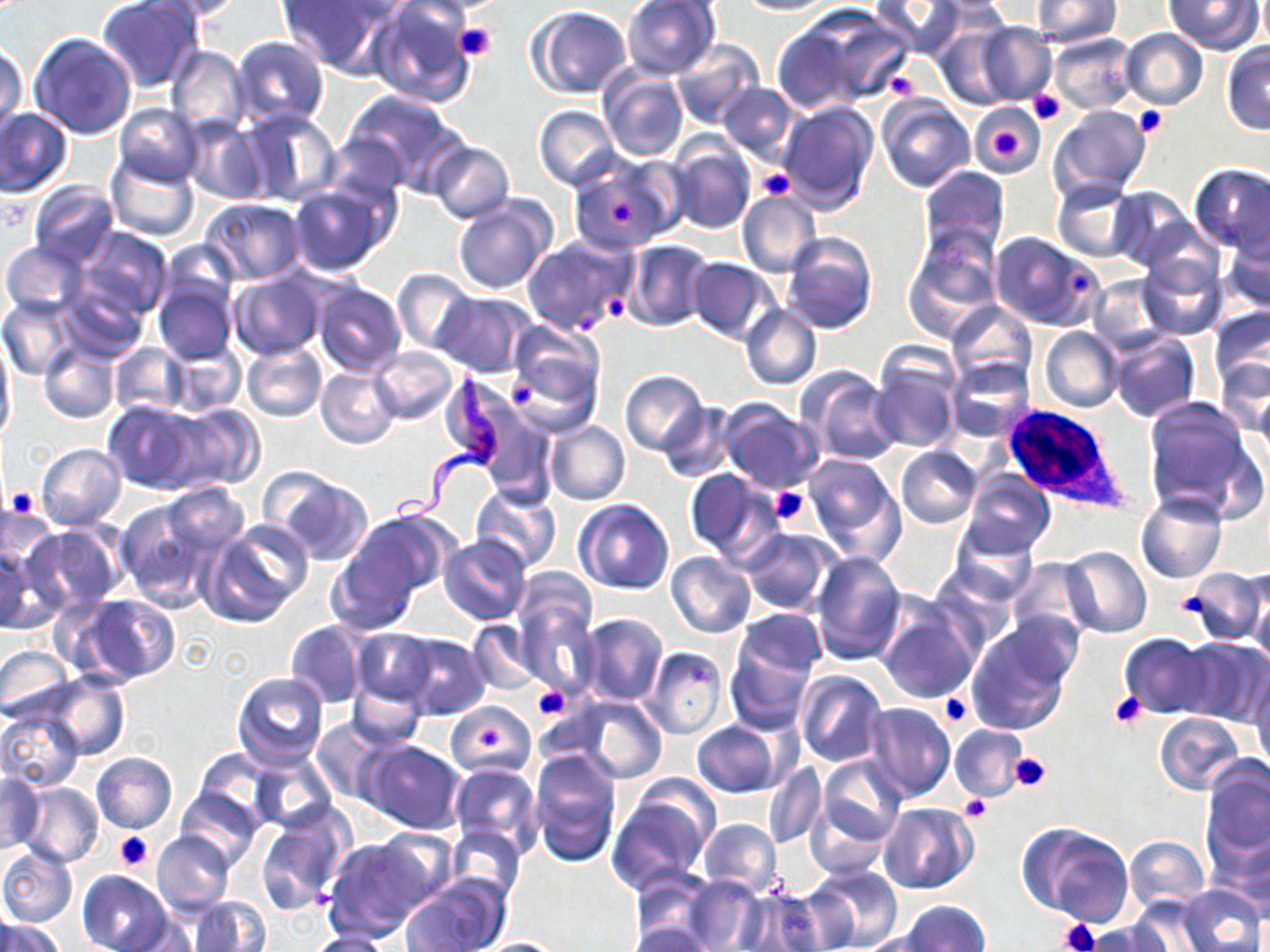
slide-level diagnosis = Trypanosoma brucei
stain = May-Grünwald-Giemsa
field of view = single
Trypanosoma brucei locations = approximate bounding boxes as named x1/y1/x2/y2 corners in pixels: (x1=388, y1=366, x2=505, y2=527)
platelet locations = approximate bounding boxes as named x1/y1/x2/y2 corners in pixels: (x1=452, y1=23, x2=497, y2=62), (x1=883, y1=67, x2=921, y2=100), (x1=1027, y1=90, x2=1064, y2=124), (x1=1133, y1=106, x2=1168, y2=139), (x1=991, y1=128, x2=1022, y2=160), (x1=755, y1=168, x2=793, y2=200), (x1=606, y1=201, x2=636, y2=225), (x1=1067, y1=269, x2=1093, y2=297), (x1=600, y1=291, x2=628, y2=323), (x1=504, y1=379, x2=541, y2=410), (x1=769, y1=486, x2=810, y2=526), (x1=6, y1=487, x2=39, y2=518), (x1=1177, y1=590, x2=1212, y2=622), (x1=531, y1=685, x2=572, y2=721), (x1=1109, y1=693, x2=1148, y2=729), (x1=939, y1=694, x2=974, y2=728), (x1=481, y1=725, x2=506, y2=749), (x1=1007, y1=752, x2=1050, y2=792), (x1=958, y1=794, x2=989, y2=823), (x1=115, y1=833, x2=152, y2=870), (x1=1058, y1=919, x2=1100, y2=952)
modality = optical microscopy
image size = 1270×952 pixels
uninfected red blood cell locations = approximate bounding boxes as named x1/y1/x2/y2 corners in pixels: (x1=96, y1=0, x2=206, y2=93), (x1=149, y1=0, x2=252, y2=20), (x1=277, y1=0, x2=394, y2=75), (x1=366, y1=0, x2=478, y2=107), (x1=621, y1=0, x2=721, y2=79), (x1=735, y1=0, x2=838, y2=16), (x1=870, y1=0, x2=964, y2=57), (x1=1030, y1=0, x2=1122, y2=46), (x1=1166, y1=0, x2=1262, y2=54), (x1=529, y1=7, x2=632, y2=99), (x1=808, y1=12, x2=913, y2=106), (x1=438, y1=19, x2=501, y2=63), (x1=967, y1=20, x2=1055, y2=105), (x1=771, y1=24, x2=866, y2=115), (x1=934, y1=24, x2=1018, y2=110), (x1=1120, y1=29, x2=1208, y2=109), (x1=28, y1=31, x2=139, y2=140), (x1=1048, y1=33, x2=1137, y2=114), (x1=231, y1=37, x2=329, y2=128), (x1=1, y1=40, x2=28, y2=139), (x1=671, y1=40, x2=764, y2=131), (x1=1220, y1=44, x2=1270, y2=135), (x1=167, y1=46, x2=249, y2=136), (x1=598, y1=70, x2=689, y2=163), (x1=717, y1=84, x2=799, y2=166), (x1=343, y1=88, x2=463, y2=188), (x1=877, y1=98, x2=974, y2=193), (x1=781, y1=101, x2=880, y2=213), (x1=114, y1=103, x2=202, y2=187), (x1=971, y1=104, x2=1045, y2=176), (x1=1046, y1=104, x2=1152, y2=202), (x1=533, y1=105, x2=620, y2=190), (x1=237, y1=107, x2=340, y2=206), (x1=0, y1=108, x2=73, y2=198), (x1=183, y1=119, x2=268, y2=205), (x1=325, y1=132, x2=408, y2=209), (x1=668, y1=140, x2=756, y2=235), (x1=427, y1=141, x2=514, y2=224), (x1=106, y1=155, x2=200, y2=243), (x1=570, y1=159, x2=681, y2=252), (x1=1187, y1=164, x2=1270, y2=252), (x1=917, y1=165, x2=1009, y2=259), (x1=1051, y1=179, x2=1138, y2=262), (x1=27, y1=182, x2=119, y2=270), (x1=287, y1=185, x2=391, y2=275), (x1=1107, y1=186, x2=1194, y2=270), (x1=738, y1=190, x2=822, y2=279), (x1=451, y1=196, x2=555, y2=295), (x1=201, y1=198, x2=306, y2=285), (x1=1143, y1=216, x2=1224, y2=297), (x1=1221, y1=219, x2=1270, y2=314), (x1=77, y1=227, x2=174, y2=318), (x1=781, y1=231, x2=879, y2=334), (x1=901, y1=231, x2=1000, y2=341), (x1=990, y1=231, x2=1101, y2=331), (x1=521, y1=235, x2=637, y2=337), (x1=161, y1=240, x2=241, y2=312), (x1=624, y1=241, x2=712, y2=331), (x1=2, y1=242, x2=88, y2=320), (x1=1138, y1=253, x2=1228, y2=340), (x1=686, y1=259, x2=778, y2=344), (x1=391, y1=269, x2=477, y2=355), (x1=227, y1=272, x2=326, y2=360), (x1=1085, y1=274, x2=1170, y2=356), (x1=57, y1=276, x2=148, y2=360), (x1=154, y1=280, x2=239, y2=365), (x1=313, y1=282, x2=405, y2=376), (x1=434, y1=292, x2=538, y2=377), (x1=0, y1=295, x2=79, y2=380), (x1=946, y1=301, x2=1037, y2=389), (x1=741, y1=303, x2=821, y2=391), (x1=1208, y1=306, x2=1270, y2=400), (x1=504, y1=319, x2=607, y2=426), (x1=1039, y1=327, x2=1124, y2=413), (x1=1107, y1=332, x2=1200, y2=424), (x1=0, y1=333, x2=15, y2=448), (x1=1122, y1=333, x2=1227, y2=474), (x1=39, y1=339, x2=119, y2=423), (x1=108, y1=342, x2=189, y2=418), (x1=242, y1=342, x2=327, y2=422), (x1=167, y1=344, x2=244, y2=415), (x1=371, y1=347, x2=458, y2=425), (x1=1214, y1=356, x2=1269, y2=437), (x1=871, y1=357, x2=960, y2=454), (x1=946, y1=357, x2=1033, y2=441), (x1=317, y1=367, x2=400, y2=449), (x1=620, y1=370, x2=709, y2=456), (x1=805, y1=373, x2=902, y2=466), (x1=1254, y1=386, x2=1270, y2=470), (x1=1143, y1=397, x2=1263, y2=520), (x1=720, y1=399, x2=824, y2=492), (x1=103, y1=401, x2=201, y2=492), (x1=165, y1=403, x2=264, y2=493), (x1=659, y1=403, x2=735, y2=482), (x1=480, y1=409, x2=557, y2=508), (x1=545, y1=422, x2=629, y2=505), (x1=35, y1=444, x2=126, y2=530), (x1=897, y1=445, x2=983, y2=530), (x1=799, y1=450, x2=905, y2=562), (x1=262, y1=468, x2=375, y2=566), (x1=682, y1=469, x2=777, y2=562), (x1=959, y1=469, x2=1054, y2=559), (x1=160, y1=483, x2=251, y2=560), (x1=471, y1=486, x2=562, y2=572), (x1=1135, y1=491, x2=1226, y2=583), (x1=575, y1=499, x2=675, y2=595), (x1=0, y1=500, x2=53, y2=590), (x1=116, y1=501, x2=219, y2=613), (x1=340, y1=512, x2=451, y2=615), (x1=203, y1=519, x2=312, y2=625), (x1=949, y1=522, x2=1040, y2=605), (x1=23, y1=524, x2=122, y2=615), (x1=738, y1=528, x2=840, y2=615), (x1=439, y1=534, x2=531, y2=625), (x1=0, y1=542, x2=47, y2=634), (x1=1060, y1=547, x2=1152, y2=638), (x1=812, y1=549, x2=907, y2=665), (x1=666, y1=553, x2=755, y2=638), (x1=1005, y1=558, x2=1094, y2=641), (x1=1180, y1=567, x2=1268, y2=644), (x1=514, y1=580, x2=599, y2=696), (x1=1251, y1=583, x2=1270, y2=673), (x1=75, y1=593, x2=181, y2=686), (x1=876, y1=601, x2=981, y2=703), (x1=735, y1=611, x2=826, y2=681), (x1=576, y1=613, x2=670, y2=707), (x1=284, y1=619, x2=367, y2=709), (x1=967, y1=621, x2=1076, y2=736), (x1=466, y1=622, x2=541, y2=696), (x1=350, y1=629, x2=438, y2=707), (x1=396, y1=633, x2=490, y2=719), (x1=1120, y1=633, x2=1215, y2=717), (x1=1179, y1=637, x2=1269, y2=727), (x1=726, y1=644, x2=817, y2=734), (x1=0, y1=645, x2=73, y2=722), (x1=643, y1=647, x2=729, y2=739), (x1=795, y1=671, x2=888, y2=768), (x1=233, y1=672, x2=327, y2=766), (x1=40, y1=674, x2=129, y2=759), (x1=1252, y1=675, x2=1270, y2=775), (x1=347, y1=680, x2=426, y2=749), (x1=797, y1=686, x2=952, y2=785), (x1=570, y1=695, x2=668, y2=785), (x1=447, y1=701, x2=536, y2=778), (x1=864, y1=701, x2=954, y2=803), (x1=0, y1=705, x2=85, y2=791), (x1=1154, y1=712, x2=1248, y2=795), (x1=312, y1=719, x2=391, y2=805), (x1=691, y1=721, x2=780, y2=797), (x1=949, y1=725, x2=1028, y2=802), (x1=360, y1=741, x2=465, y2=833), (x1=193, y1=749, x2=271, y2=826), (x1=530, y1=750, x2=622, y2=865), (x1=91, y1=752, x2=177, y2=835), (x1=248, y1=754, x2=337, y2=834), (x1=817, y1=756, x2=906, y2=850), (x1=1201, y1=758, x2=1270, y2=872), (x1=763, y1=761, x2=826, y2=849), (x1=449, y1=764, x2=542, y2=854), (x1=0, y1=773, x2=43, y2=855), (x1=622, y1=773, x2=722, y2=865), (x1=17, y1=781, x2=103, y2=868), (x1=177, y1=789, x2=261, y2=870), (x1=606, y1=797, x2=709, y2=894), (x1=879, y1=802, x2=978, y2=893), (x1=255, y1=807, x2=353, y2=917), (x1=1208, y1=817, x2=1270, y2=911), (x1=698, y1=818, x2=781, y2=895), (x1=1019, y1=823, x2=1135, y2=927), (x1=445, y1=827, x2=526, y2=904), (x1=371, y1=829, x2=460, y2=910), (x1=153, y1=831, x2=236, y2=918), (x1=1123, y1=836, x2=1209, y2=909), (x1=324, y1=838, x2=430, y2=939), (x1=0, y1=845, x2=77, y2=928), (x1=805, y1=865, x2=904, y2=950), (x1=629, y1=867, x2=715, y2=943), (x1=77, y1=871, x2=174, y2=952), (x1=401, y1=876, x2=508, y2=952), (x1=683, y1=876, x2=763, y2=950), (x1=1178, y1=885, x2=1264, y2=952), (x1=736, y1=889, x2=831, y2=951), (x1=1130, y1=893, x2=1221, y2=950), (x1=188, y1=895, x2=271, y2=952), (x1=901, y1=901, x2=991, y2=952), (x1=0, y1=916, x2=65, y2=952), (x1=1081, y1=920, x2=1170, y2=951), (x1=628, y1=921, x2=710, y2=952), (x1=860, y1=932, x2=944, y2=952), (x1=307, y1=933, x2=394, y2=952), (x1=478, y1=938, x2=568, y2=951)
white blood cell locations = approximate bounding boxes as named x1/y1/x2/y2 corners in pixels: (x1=1004, y1=407, x2=1128, y2=516)
magnification = 1000x
preparation = thin blood film